Describe the morphology of the red blood cells.
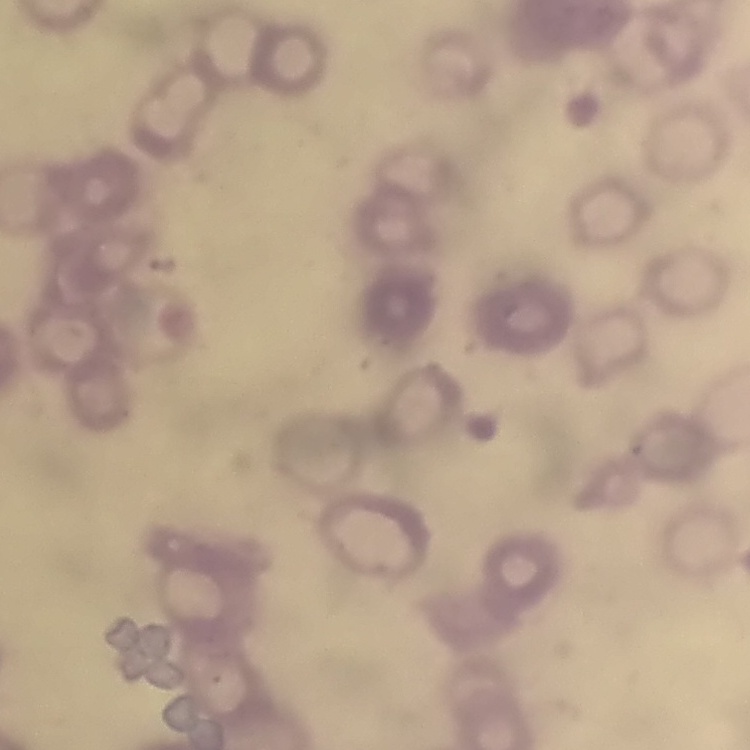

Rouleaux formation.

image_type: square crop of a larger photomicrograph
stain: Field's or Giemsa
preparation: thin blood film